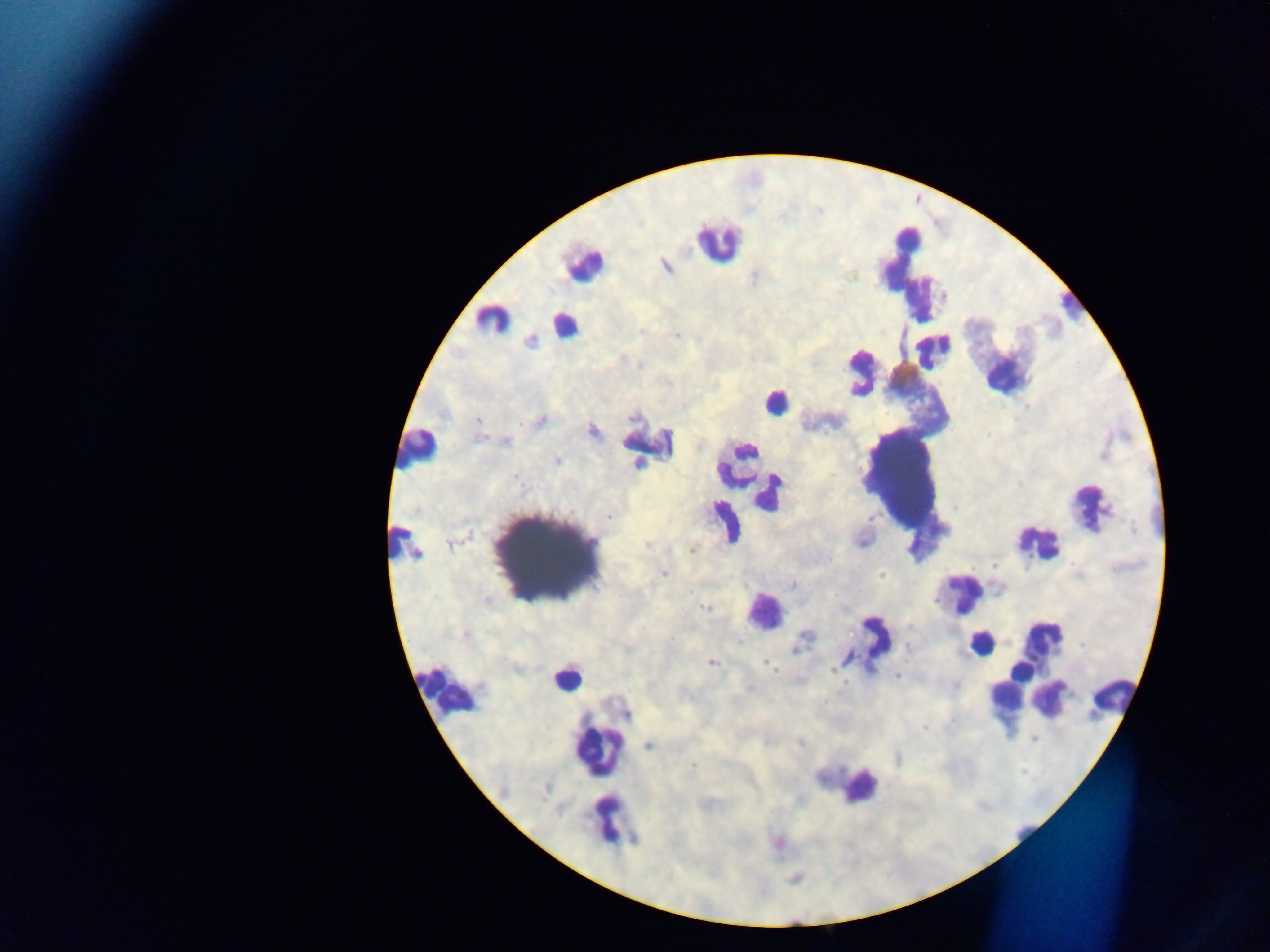
Approximate centers as (x, y) in pixels. Plasmodium parasite locations: (665, 265), (755, 276), (641, 330), (677, 335), (529, 339), (540, 419), (478, 420), (591, 430), (505, 441), (557, 460), (609, 517), (871, 518), (646, 544), (692, 550), (993, 565), (664, 574), (881, 574), (792, 585), (486, 599), (705, 607), (1082, 645), (908, 646), (710, 661), (767, 661), (770, 667), (774, 670), (897, 675), (845, 681), (923, 726), (1034, 739), (799, 742), (649, 744), (898, 758), (691, 766), (777, 843). Leukocyte locations: (907, 241), (718, 242), (583, 263), (905, 267), (919, 297), (1071, 304), (492, 319), (565, 324), (934, 350), (861, 371), (1007, 373), (775, 402), (649, 443), (417, 448), (740, 468), (904, 475), (756, 484), (768, 493), (1090, 506), (724, 522), (1038, 542), (402, 544), (547, 556), (960, 593), (764, 611), (875, 639), (1041, 639), (981, 642), (1020, 672), (566, 677), (1008, 688), (446, 690), (1032, 691), (1112, 694), (1049, 697), (598, 751), (860, 786), (612, 821), (1026, 828). Image is 1270×952 pixels. Thick blood film. Sample from Ghana. Mobile-phone photograph taken through the microscope. Single field of view.